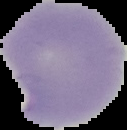 Cell region segmented out of the field of view; the surrounding area is masked to black. Image is 127×130 pixels. Result: negative for malaria parasites. From a thin blood smear.